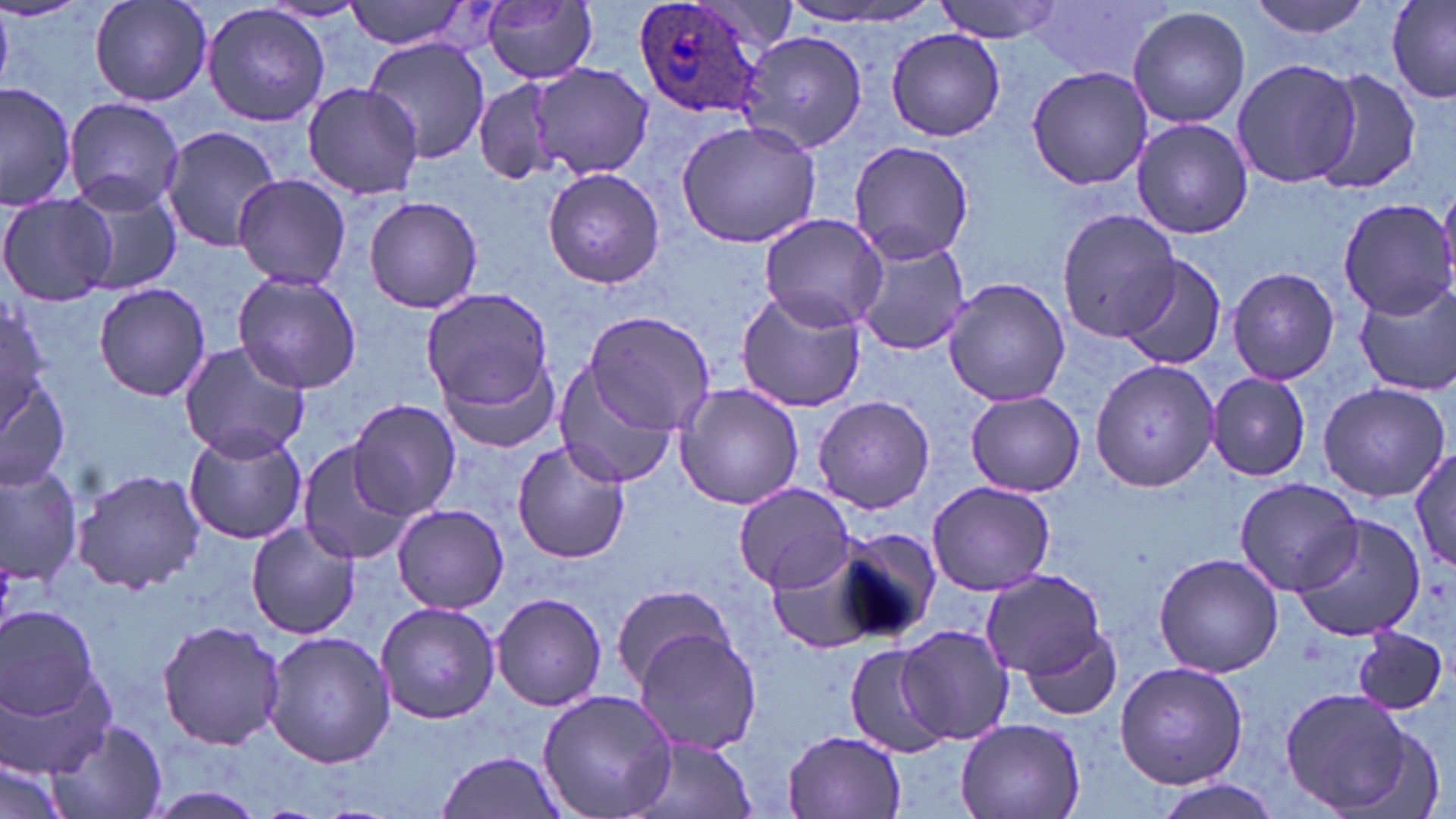
Summary:
  - Coordinate format: approximate bounding boxes as (x1,y1)-(x2,y2) corner pairs in pixels
  - Uninfected red blood cell locations: (87,0)-(213,109), (343,0)-(479,52), (781,0)-(944,30), (933,0)-(1062,43), (1241,0)-(1383,40), (1386,0)-(1456,103), (482,1)-(600,85), (257,2)-(374,25), (1029,2)-(1172,82), (201,4)-(332,127), (1126,5)-(1251,129), (885,28)-(1007,141), (741,30)-(870,151), (364,37)-(489,165), (1230,56)-(1360,191), (530,64)-(654,180), (1027,65)-(1153,192), (1311,69)-(1423,194), (471,76)-(568,188), (0,80)-(77,211), (303,83)-(420,199), (63,97)-(185,216), (1130,116)-(1252,239), (677,119)-(821,247), (160,125)-(283,251), (847,140)-(975,264), (543,168)-(665,289), (231,174)-(353,289), (72,180)-(183,297), (0,193)-(116,306), (362,194)-(483,314), (1338,197)-(1456,318), (1056,211)-(1177,346), (757,214)-(889,333), (853,236)-(974,357), (1116,253)-(1228,370), (1226,267)-(1340,386), (232,270)-(365,394), (943,278)-(1070,408), (1354,281)-(1456,395), (94,282)-(213,401), (419,286)-(554,412), (736,290)-(867,414), (0,301)-(50,423), (583,312)-(716,436), (178,340)-(311,461), (1090,356)-(1219,493), (443,360)-(563,455), (0,362)-(73,493), (552,363)-(677,489), (1207,373)-(1311,481), (1317,381)-(1451,502), (674,383)-(806,511), (964,391)-(1086,497), (812,394)-(936,514), (348,398)-(461,519), (183,427)-(308,544), (295,440)-(415,565), (511,440)-(629,564), (1412,448)-(1456,573), (0,461)-(83,590), (72,467)-(206,593), (1233,477)-(1363,595), (926,481)-(1058,598), (734,483)-(854,593), (392,503)-(509,612), (1289,514)-(1428,643), (246,523)-(361,638), (831,526)-(942,644), (765,546)-(889,656), (1153,552)-(1284,679), (980,570)-(1105,677), (609,585)-(738,688), (492,592)-(607,711), (375,601)-(503,724), (0,606)-(102,723), (156,619)-(288,751), (895,625)-(1015,748), (1020,625)-(1122,721), (1354,625)-(1447,715), (632,627)-(762,757), (263,632)-(396,768), (845,643)-(951,760), (1,647)-(120,781), (1116,661)-(1248,791), (1278,686)-(1427,817), (537,688)-(679,819), (955,718)-(1085,819), (47,719)-(168,818), (782,730)-(906,818), (627,737)-(757,819), (433,750)-(566,819), (1,758)-(71,819), (1152,777)-(1282,819), (136,785)-(271,816)
  - Plasmodium ovale-infected red blood cell locations: (630,0)-(771,120)
  - Slide-level diagnosis: Plasmodium ovale
  - Preparation: thin blood film
  - Magnification: 1000x
  - Field of view: one of a larger specimen
  - Modality: light microscopy
  - Stain: May-Grünwald-Giemsa
  - Image size: 1456×819 pixels